Name the blood parasite species.
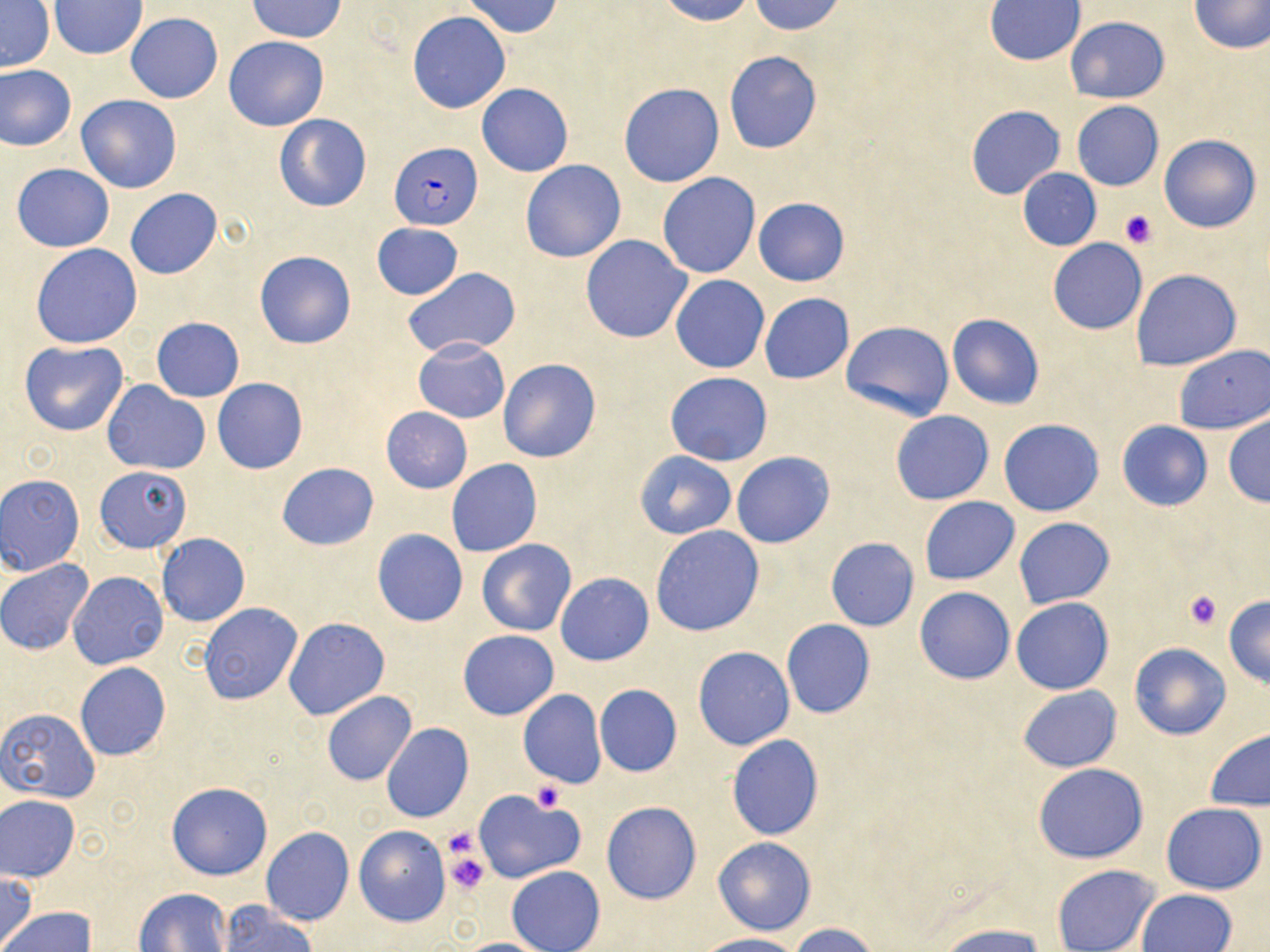

Plasmodium falciparum.

Summary:
  - Coordinate format: approximate bounding boxes as named x1/y1/x2/y2 corners in pixels
  - Plasmodium falciparum-infected red blood cell locations: (x1=389, y1=140, x2=481, y2=230)
  - Uninfected red blood cell locations: (x1=247, y1=0, x2=346, y2=42), (x1=463, y1=0, x2=563, y2=37), (x1=656, y1=0, x2=756, y2=25), (x1=748, y1=0, x2=846, y2=35), (x1=1188, y1=0, x2=1269, y2=55), (x1=1, y1=1, x2=56, y2=73), (x1=49, y1=1, x2=146, y2=59), (x1=984, y1=1, x2=1086, y2=66), (x1=125, y1=12, x2=223, y2=103), (x1=407, y1=12, x2=511, y2=113), (x1=1066, y1=16, x2=1170, y2=102), (x1=224, y1=36, x2=329, y2=131), (x1=724, y1=50, x2=822, y2=154), (x1=0, y1=64, x2=77, y2=151), (x1=618, y1=82, x2=725, y2=187), (x1=477, y1=83, x2=573, y2=176), (x1=76, y1=94, x2=182, y2=194), (x1=1071, y1=101, x2=1164, y2=191), (x1=966, y1=106, x2=1065, y2=200), (x1=274, y1=113, x2=372, y2=213), (x1=1159, y1=134, x2=1261, y2=234), (x1=521, y1=160, x2=626, y2=263), (x1=11, y1=163, x2=114, y2=252), (x1=1018, y1=168, x2=1101, y2=250), (x1=658, y1=172, x2=760, y2=278), (x1=125, y1=188, x2=223, y2=280), (x1=753, y1=197, x2=850, y2=285), (x1=372, y1=222, x2=463, y2=300), (x1=580, y1=234, x2=693, y2=343), (x1=1048, y1=238, x2=1147, y2=334), (x1=31, y1=244, x2=143, y2=349), (x1=254, y1=250, x2=356, y2=350), (x1=402, y1=268, x2=521, y2=358), (x1=1131, y1=268, x2=1243, y2=371), (x1=671, y1=274, x2=769, y2=373), (x1=759, y1=292, x2=855, y2=383), (x1=946, y1=314, x2=1045, y2=409), (x1=152, y1=317, x2=244, y2=402), (x1=840, y1=320, x2=955, y2=421), (x1=413, y1=337, x2=510, y2=423), (x1=19, y1=340, x2=129, y2=436), (x1=1172, y1=345, x2=1269, y2=435), (x1=498, y1=359, x2=601, y2=462), (x1=665, y1=372, x2=772, y2=466), (x1=212, y1=378, x2=308, y2=474), (x1=101, y1=381, x2=210, y2=475), (x1=381, y1=406, x2=472, y2=493), (x1=891, y1=411, x2=993, y2=504), (x1=1223, y1=414, x2=1270, y2=507), (x1=999, y1=419, x2=1104, y2=517), (x1=1116, y1=420, x2=1213, y2=511), (x1=635, y1=452, x2=736, y2=539), (x1=731, y1=452, x2=835, y2=549), (x1=446, y1=459, x2=542, y2=557), (x1=276, y1=462, x2=379, y2=550), (x1=95, y1=467, x2=190, y2=553), (x1=0, y1=474, x2=85, y2=575), (x1=920, y1=496, x2=1019, y2=583), (x1=1014, y1=518, x2=1115, y2=609), (x1=650, y1=525, x2=764, y2=636), (x1=373, y1=528, x2=467, y2=627), (x1=156, y1=533, x2=250, y2=627), (x1=826, y1=538, x2=919, y2=631), (x1=477, y1=539, x2=576, y2=636), (x1=1, y1=558, x2=94, y2=655), (x1=69, y1=572, x2=169, y2=671), (x1=556, y1=573, x2=654, y2=666), (x1=915, y1=586, x2=1015, y2=684), (x1=1223, y1=595, x2=1270, y2=688), (x1=1011, y1=597, x2=1115, y2=695), (x1=198, y1=603, x2=301, y2=705), (x1=284, y1=617, x2=389, y2=720), (x1=781, y1=619, x2=875, y2=718), (x1=457, y1=630, x2=559, y2=721), (x1=1128, y1=642, x2=1231, y2=739), (x1=693, y1=646, x2=795, y2=750), (x1=76, y1=663, x2=172, y2=760), (x1=595, y1=684, x2=682, y2=777), (x1=1018, y1=686, x2=1121, y2=772), (x1=517, y1=689, x2=606, y2=789), (x1=321, y1=691, x2=417, y2=787), (x1=1, y1=708, x2=102, y2=803), (x1=381, y1=723, x2=474, y2=824), (x1=1204, y1=728, x2=1270, y2=811), (x1=726, y1=735, x2=824, y2=841), (x1=1033, y1=764, x2=1148, y2=863), (x1=166, y1=781, x2=273, y2=880), (x1=473, y1=790, x2=587, y2=883), (x1=1, y1=795, x2=80, y2=881), (x1=601, y1=801, x2=701, y2=904), (x1=1161, y1=802, x2=1267, y2=894), (x1=354, y1=826, x2=450, y2=927), (x1=260, y1=827, x2=355, y2=926), (x1=712, y1=837, x2=817, y2=935), (x1=1051, y1=864, x2=1161, y2=952), (x1=507, y1=866, x2=605, y2=952), (x1=0, y1=870, x2=38, y2=949), (x1=135, y1=888, x2=232, y2=952), (x1=1137, y1=889, x2=1238, y2=952), (x1=217, y1=902, x2=315, y2=951), (x1=0, y1=906, x2=97, y2=951), (x1=788, y1=922, x2=884, y2=952), (x1=936, y1=923, x2=1051, y2=952), (x1=698, y1=934, x2=803, y2=952), (x1=452, y1=937, x2=553, y2=951)
  - Platelet locations: (x1=1118, y1=208, x2=1159, y2=249), (x1=1182, y1=589, x2=1223, y2=630), (x1=532, y1=782, x2=565, y2=811), (x1=443, y1=850, x2=490, y2=895)
  - Preparation: thin blood smear
  - Stain: May-Grünwald-Giemsa
  - Magnification: 1000x
  - Modality: light microscopy
  - Field of view: one of a larger specimen
  - Image size: 1270×952 pixels